Describe the morphology of the red blood cells.
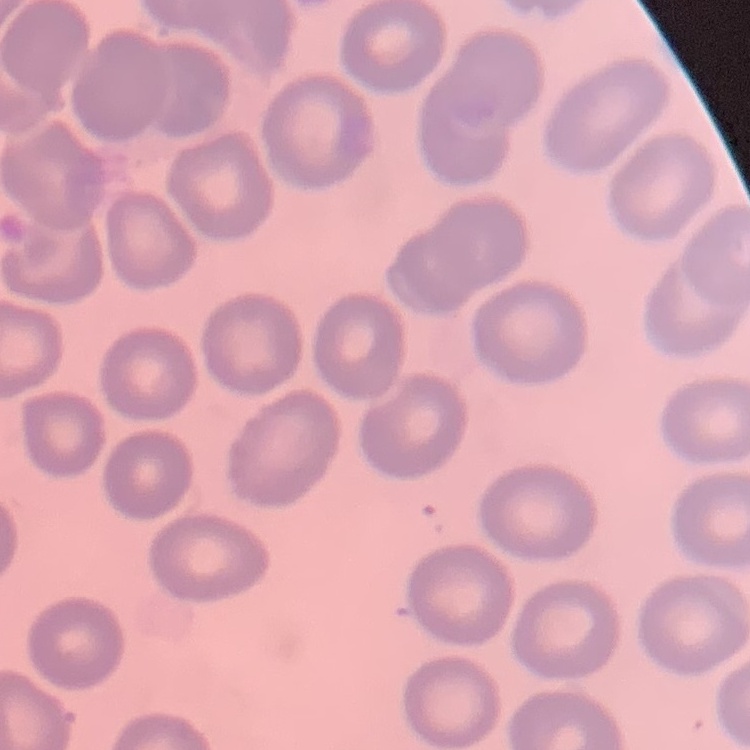
They show no rouleaux formation.

Summary:
  - Stain: Field's or Giemsa
  - Preparation: thin blood smear
  - Image type: square crop of a larger photomicrograph